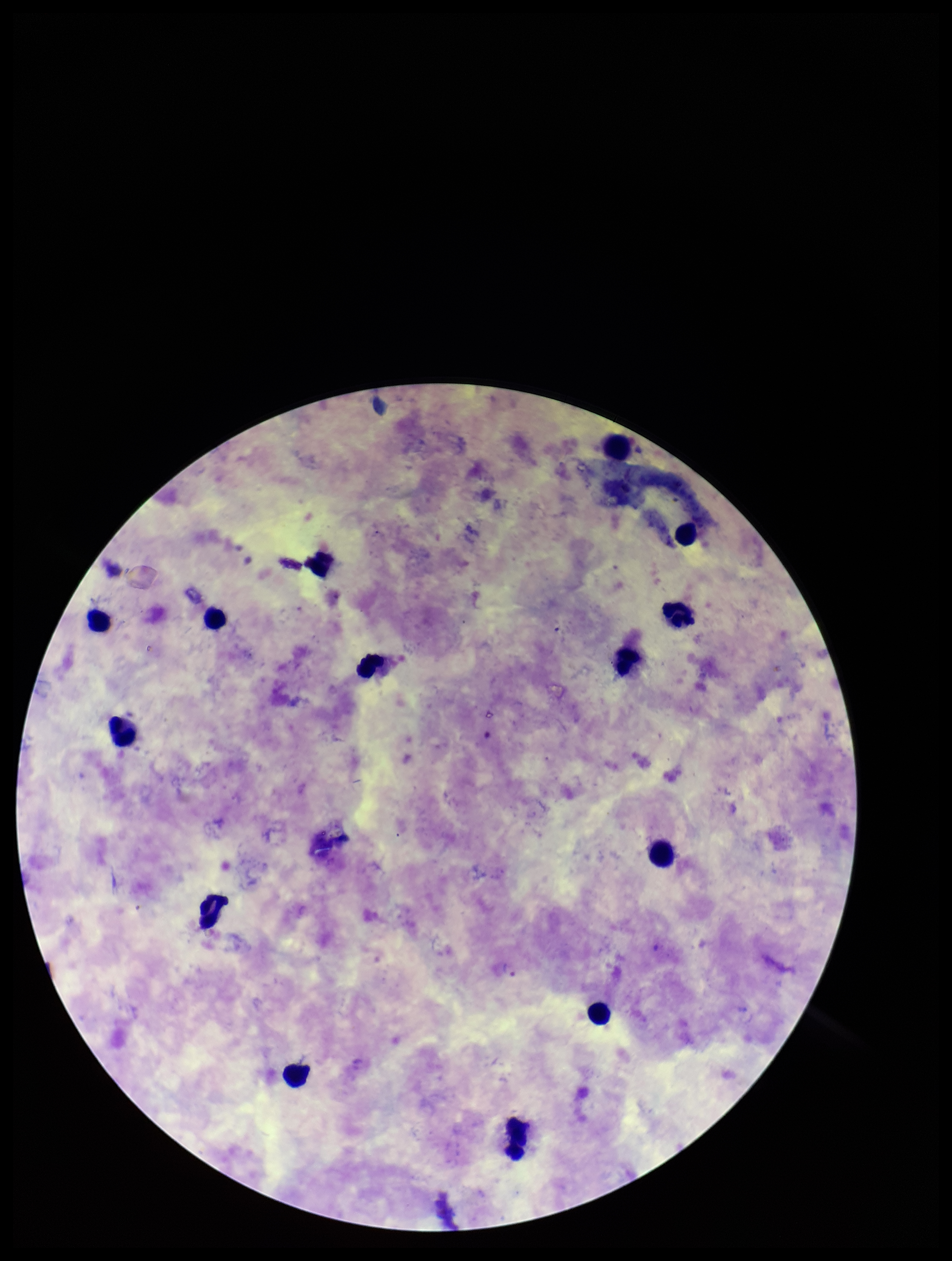
Image is 952×1261 pixels. Leukocyte count: 14. Species reported for this patient: Plasmodium vivax. Preparation: thick blood smear. One field from this slide. Photographed through the microscope eyepiece with a smartphone camera. Patient malaria status: positive. Giemsa stain. Parasite count: 1. Plasmodium parasites: seen.